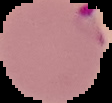
From a thin blood film. Cell region segmented out of the field of view; the surrounding area is masked to black. Image is 112×103 pixels. Malaria status: parasitized.